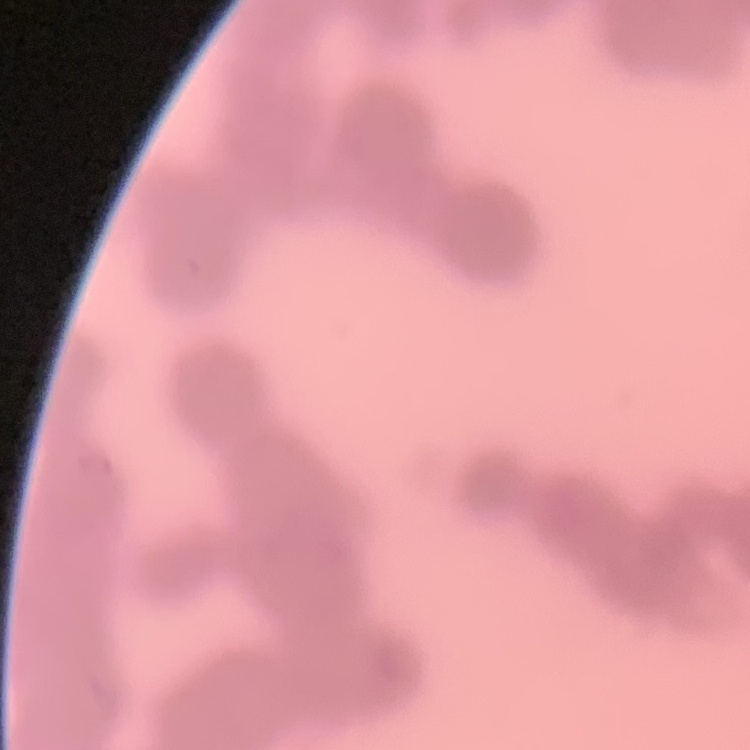
Summary:
  - Red blood cell morphology: rouleaux formation
  - Stain: Field's or Giemsa
  - Image type: square crop of a larger photomicrograph
  - Preparation: thin blood film